Name the blood parasite species.
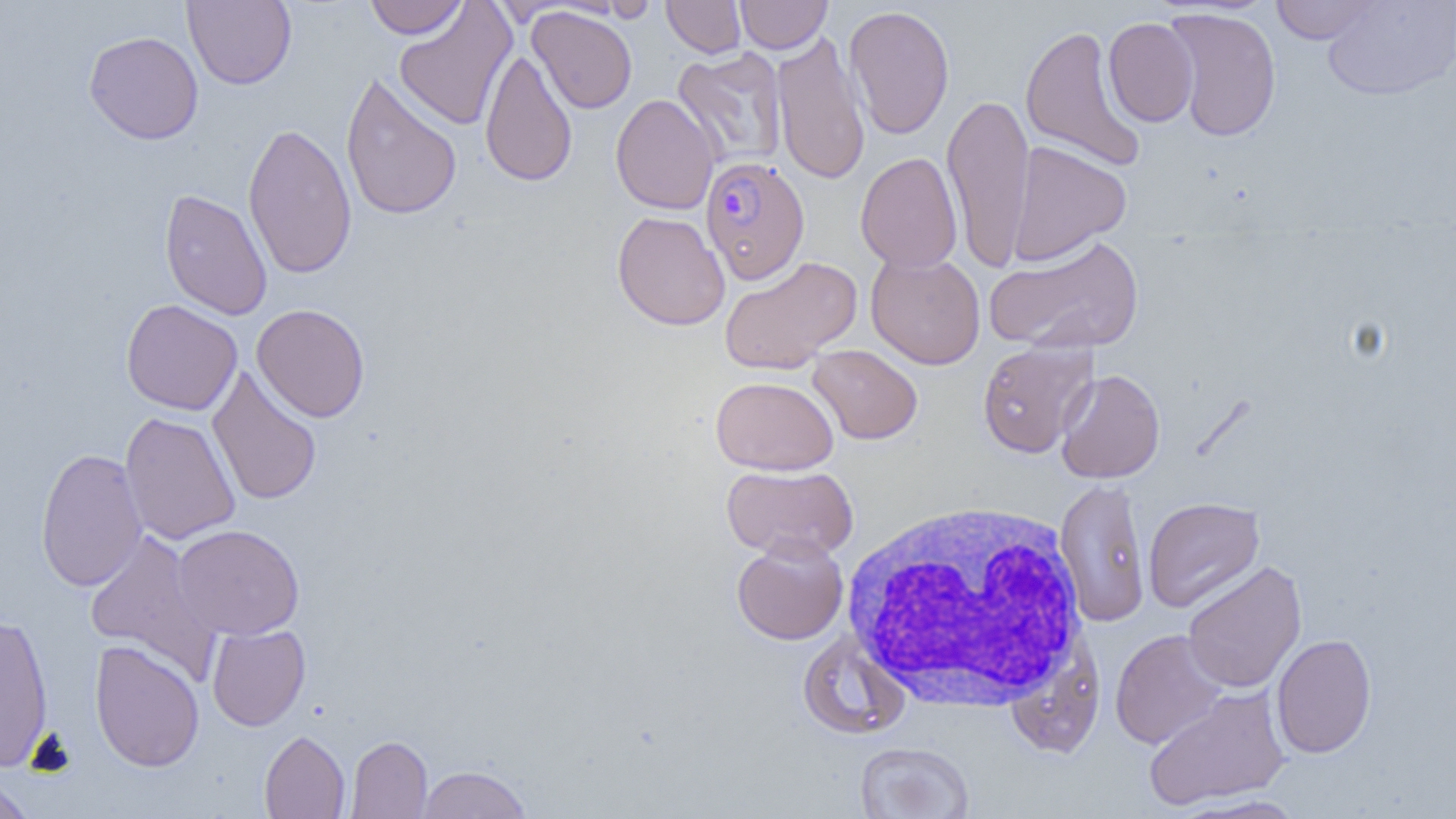

Plasmodium falciparum.

Summary:
  - Coordinate format: approximate bounding boxes as (x1, y1, x2, y2) in pixels
  - Uninfected red blood cell locations: (182, 0, 297, 89), (364, 0, 468, 39), (601, 0, 658, 23), (662, 0, 746, 58), (735, 0, 832, 53), (1321, 0, 1456, 101), (1269, 1, 1382, 44), (394, 2, 516, 131), (844, 5, 955, 140), (527, 6, 637, 113), (1163, 7, 1283, 142), (1103, 17, 1199, 127), (1019, 23, 1147, 173), (83, 30, 204, 144), (770, 31, 870, 186), (480, 48, 578, 188), (672, 48, 788, 170), (340, 72, 463, 222), (942, 92, 1035, 271), (610, 93, 720, 215), (242, 121, 357, 280), (1007, 140, 1131, 266), (855, 152, 963, 272), (159, 188, 273, 320), (612, 211, 730, 331), (984, 233, 1145, 356), (865, 251, 986, 369), (718, 255, 862, 375), (121, 299, 242, 415), (252, 303, 370, 423), (977, 340, 1097, 458), (807, 345, 922, 445), (207, 365, 322, 506), (1055, 369, 1166, 483), (711, 376, 839, 475), (120, 412, 240, 545), (35, 447, 148, 591), (721, 464, 858, 561), (1055, 477, 1151, 627), (1143, 496, 1265, 612), (172, 524, 304, 641), (83, 530, 221, 681), (731, 536, 848, 645), (1182, 561, 1307, 694), (0, 612, 54, 771), (207, 623, 310, 731), (1110, 629, 1228, 749), (797, 633, 910, 740), (1271, 633, 1377, 758), (89, 640, 205, 772), (1005, 640, 1106, 758), (1142, 686, 1290, 811), (259, 730, 350, 818), (345, 735, 432, 819), (854, 741, 974, 818), (417, 764, 531, 818), (0, 774, 35, 819), (1169, 794, 1310, 818)
  - White blood cell locations: (839, 498, 1090, 712)
  - Plasmodium falciparum-infected red blood cell locations: (700, 156, 810, 285)
  - Field of view: one of a larger specimen
  - Preparation: thin blood film
  - Magnification: 1000x
  - Modality: optical microscopy
  - Image size: 1456×819 pixels